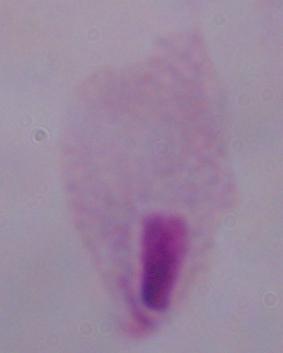

Summary:
  - Modality: micrograph
  - Magnification: 1000x
  - Identification: trichomonad